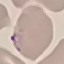

Summary:
  - Result: malaria parasites identified
  - Preparation: thin blood smear
  - Image type: cell patch, automatically extracted from a larger field of view and resized to 64 × 64 pixels
  - Stain: Giemsa
  - Capture: smartphone camera at the microscope eyepiece